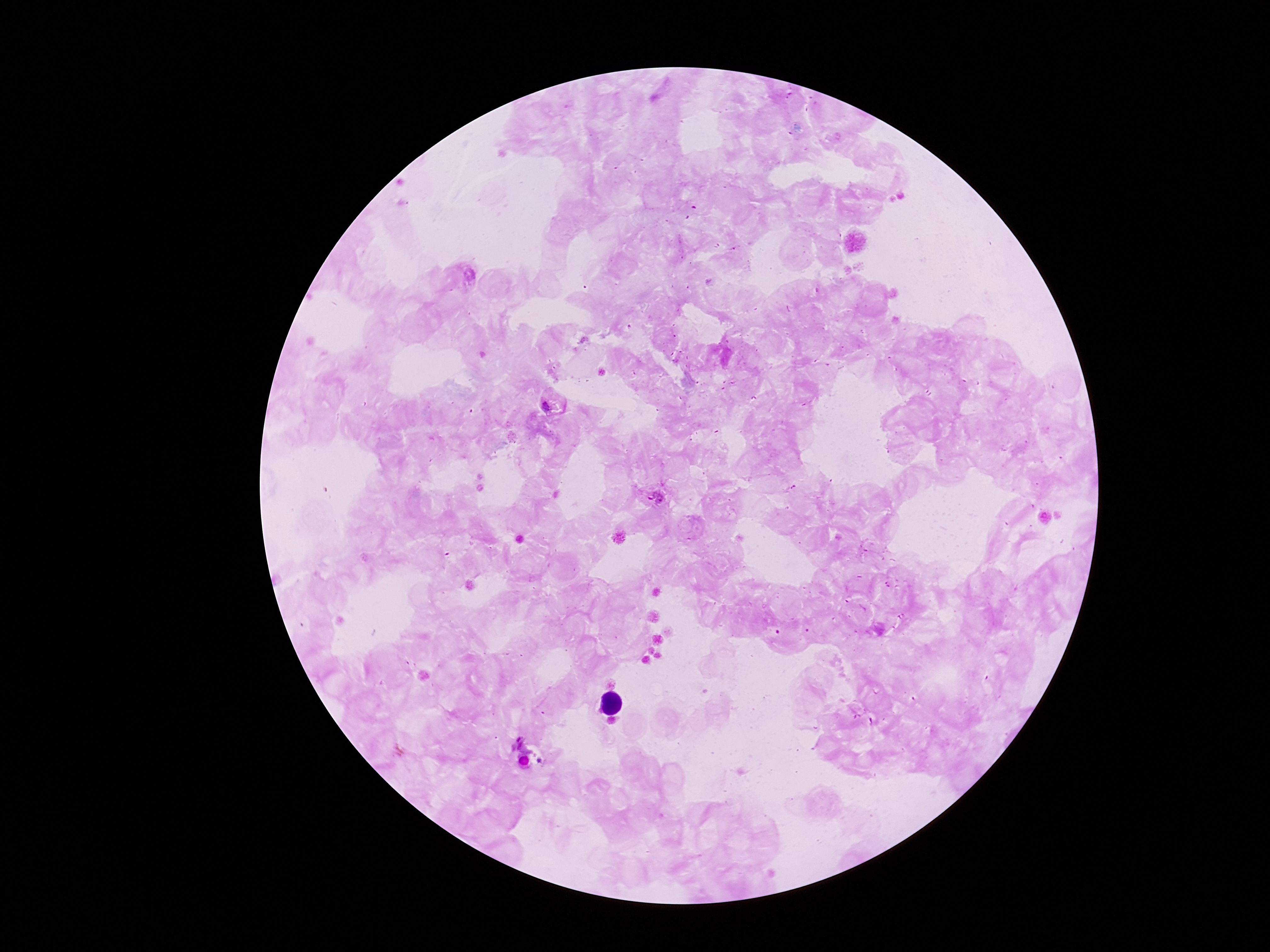

Approximate centers as {x, y} in pixels. Plasmodium parasite locations: {553, 404}, {654, 495}. 100x magnification. Patient malaria status: infected. Thick blood smear. Photographed through the microscope eyepiece with a smartphone camera. Giemsa stain. Single field of view. Image is 1270×952 pixels.